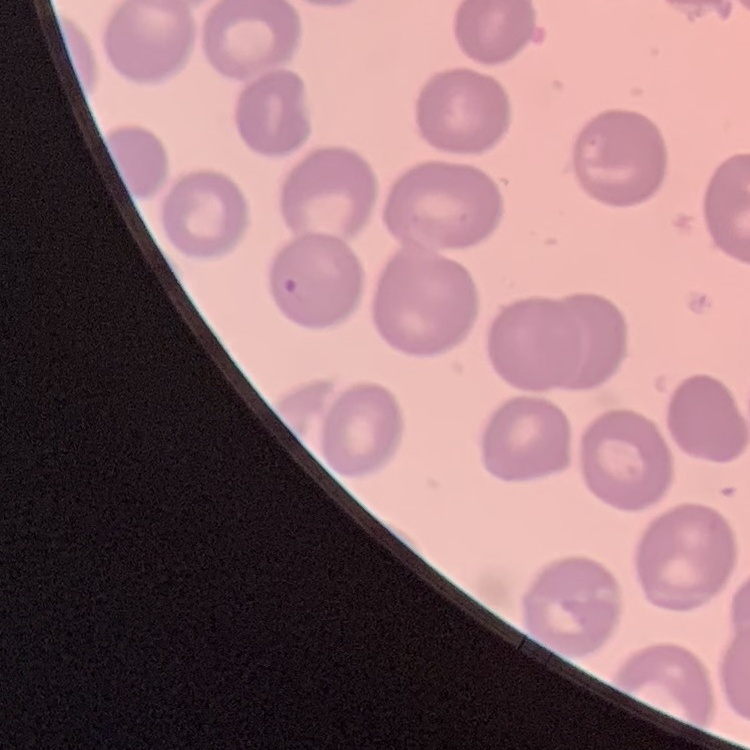
red blood cell morphology = no rouleaux formation
preparation = thin blood smear
stain = Field's or Giemsa
image type = one tile cut from a larger photomicrograph